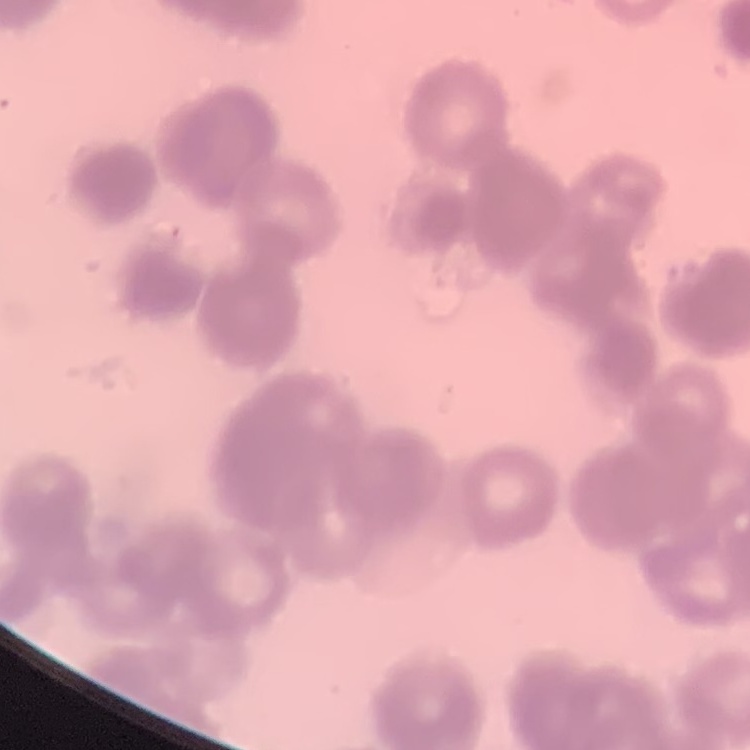

red blood cell morphology = rouleaux formation
preparation = thin peripheral smear
stain = Field's or Giemsa
image type = one tile cut from a larger photomicrograph